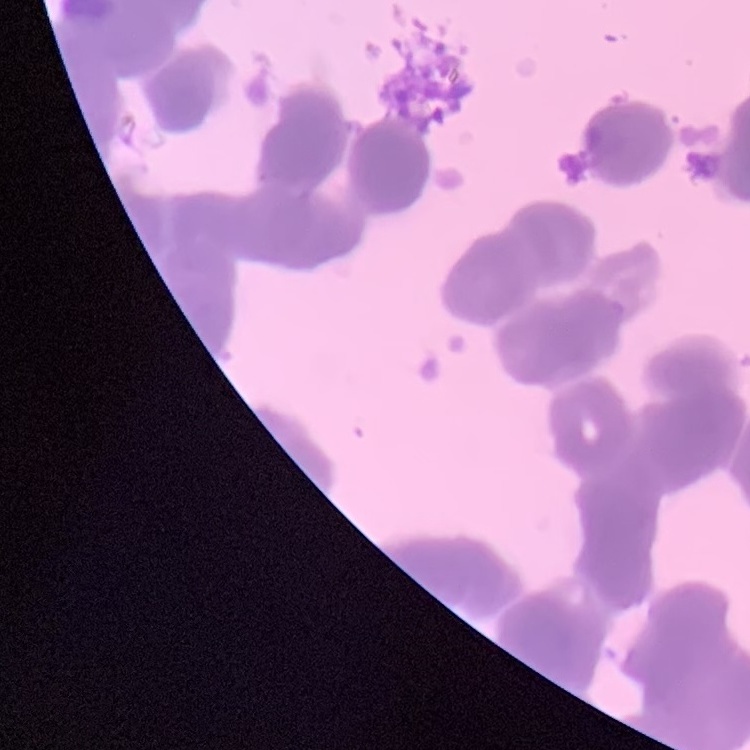

erythrocyte morphology = rouleaux formation
image type = one tile cut from a larger photomicrograph
preparation = thin peripheral smear
stain = Field's or Giemsa